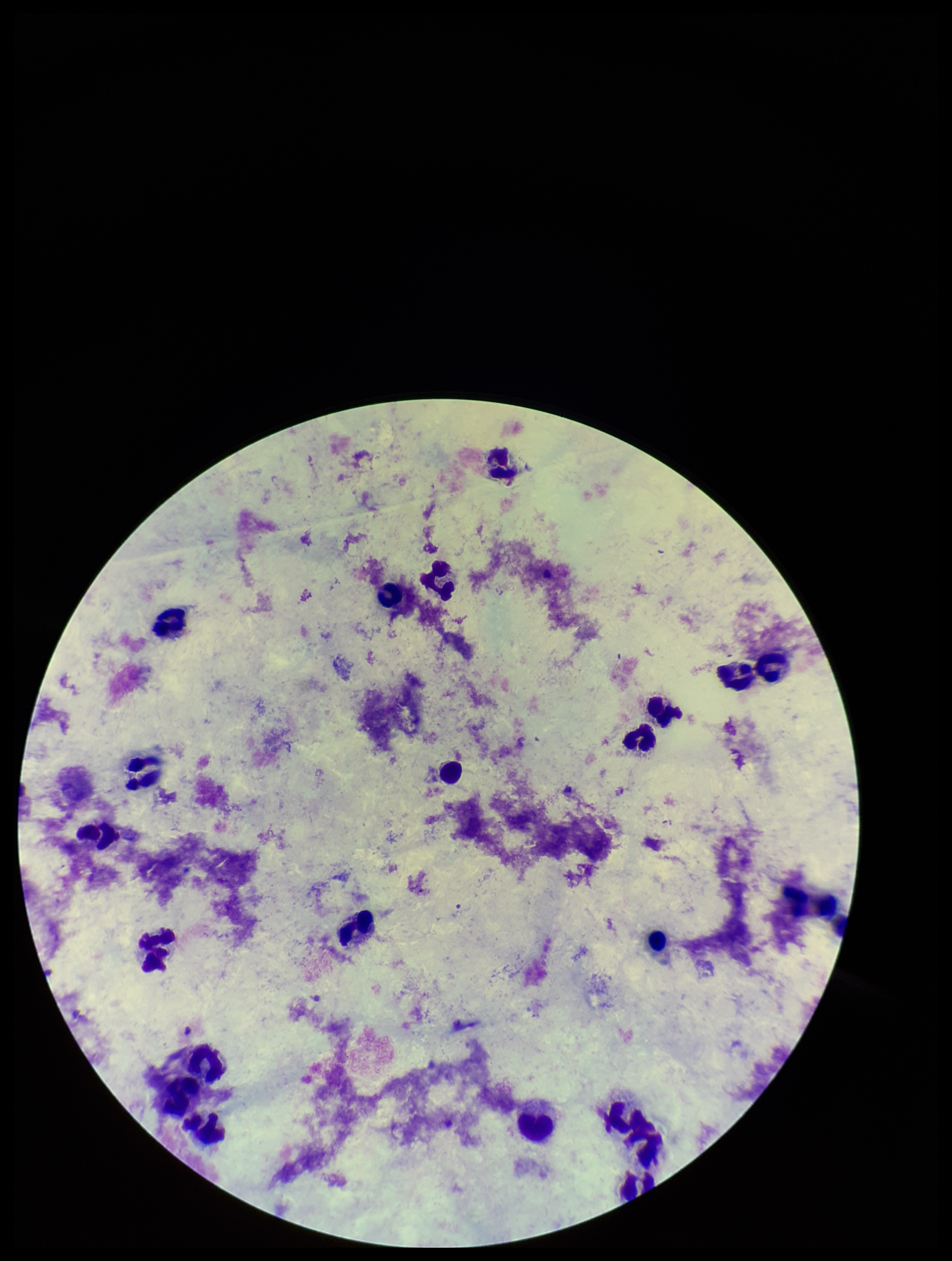
patient malaria status = negative
parasite count = 0
Plasmodium parasites = none detected
capture = smartphone photograph through the microscope eyepiece
image size = 952×1261 pixels
leukocyte count = 22
stain = Giemsa
field of view = one from this slide
preparation = thick